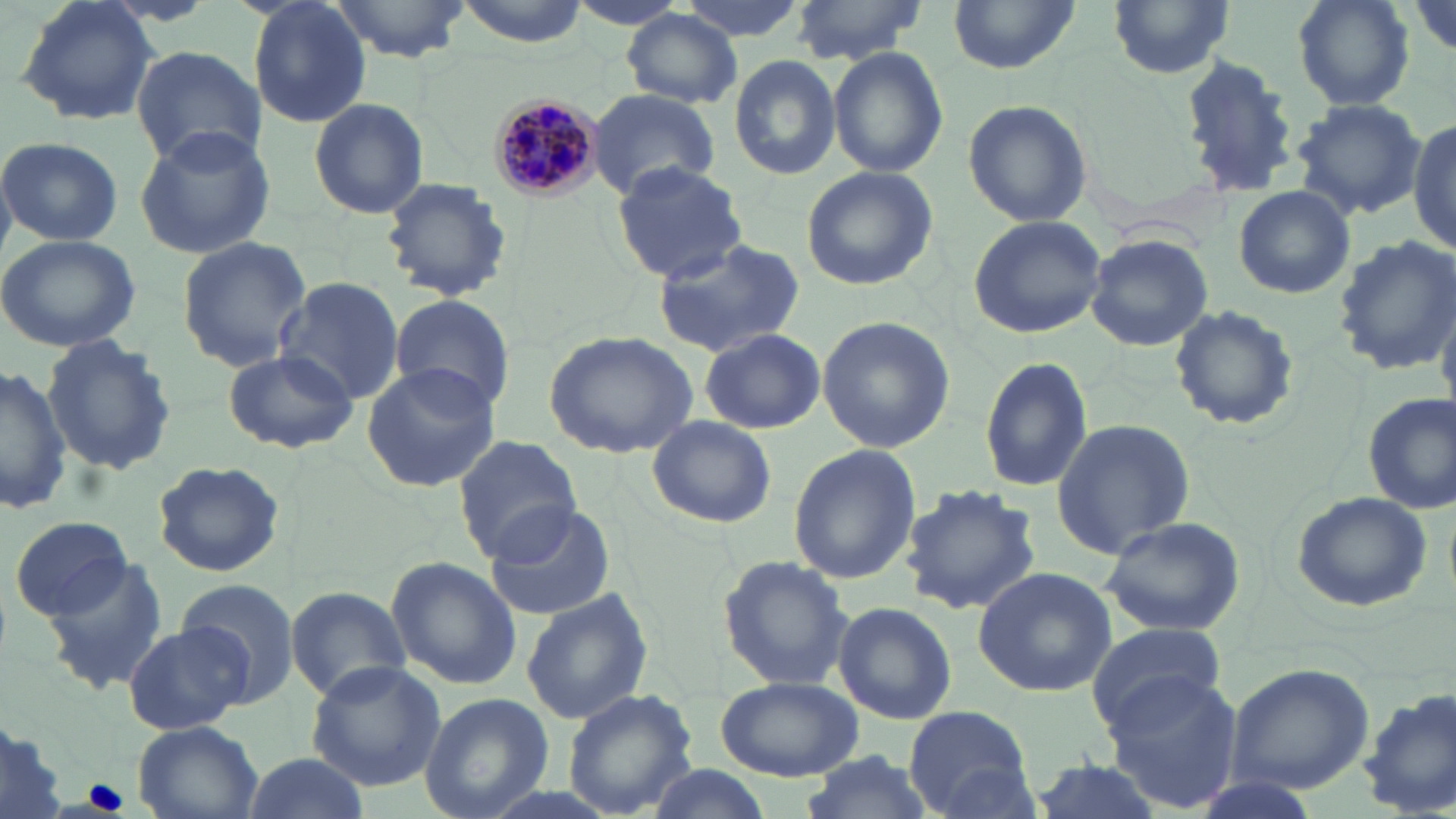

slide-level diagnosis = Plasmodium malariae
field of view = one of a larger specimen
stain = May-Grünwald-Giemsa
magnification = 1000x
preparation = thin blood film
modality = optical microscopy
Plasmodium malariae-infected red blood cell locations = approximate bounding boxes as [x1, y1, x2, y2] in pixels: [487, 92, 605, 201]
uninfected red blood cell locations = approximate bounding boxes as [x1, y1, x2, y2] in pixels: [15, 0, 162, 127], [247, 0, 373, 130], [333, 0, 468, 56], [450, 0, 595, 46], [672, 0, 811, 41], [787, 0, 932, 64], [949, 0, 1080, 75], [1109, 0, 1236, 79], [1290, 0, 1415, 112], [622, 10, 741, 108], [130, 45, 266, 170], [828, 46, 949, 178], [1177, 54, 1301, 199], [730, 55, 842, 180], [585, 89, 719, 201], [308, 98, 432, 220], [1291, 98, 1427, 217], [961, 99, 1093, 228], [1409, 116, 1456, 255], [133, 125, 277, 260], [2, 138, 123, 246], [610, 160, 746, 282], [800, 166, 942, 293], [378, 177, 513, 302], [1233, 185, 1356, 299], [967, 214, 1107, 339], [1085, 232, 1213, 353], [0, 233, 141, 353], [1333, 234, 1456, 376], [176, 236, 313, 373], [649, 237, 807, 358], [275, 278, 404, 404], [387, 292, 514, 413], [1167, 304, 1300, 432], [816, 316, 955, 454], [699, 328, 827, 435], [543, 331, 699, 460], [39, 335, 178, 478], [223, 346, 358, 454], [979, 354, 1094, 495], [359, 361, 504, 493], [0, 366, 72, 513], [1360, 394, 1455, 516], [646, 415, 776, 529], [1049, 417, 1196, 560], [1327, 425, 1449, 587], [452, 435, 584, 562], [787, 445, 921, 584], [151, 461, 290, 577], [900, 485, 1041, 617], [1289, 491, 1433, 612], [485, 501, 618, 621], [10, 514, 132, 622], [1098, 515, 1247, 637], [716, 553, 856, 694], [40, 556, 168, 694], [386, 557, 520, 692], [972, 566, 1116, 696], [176, 580, 302, 704], [284, 585, 407, 702], [520, 588, 656, 726], [833, 602, 957, 724], [122, 620, 252, 734], [1085, 623, 1227, 734], [1225, 660, 1377, 795], [305, 661, 446, 792], [1102, 670, 1245, 814], [713, 674, 862, 780], [560, 687, 699, 819], [1358, 688, 1456, 819], [418, 693, 551, 818], [904, 706, 1034, 817], [0, 716, 70, 819], [132, 720, 265, 819], [242, 751, 370, 818], [796, 751, 935, 819], [1026, 757, 1167, 819], [643, 763, 774, 818]
image size = 1456×819 pixels